Assess the morphology of the red blood cells.
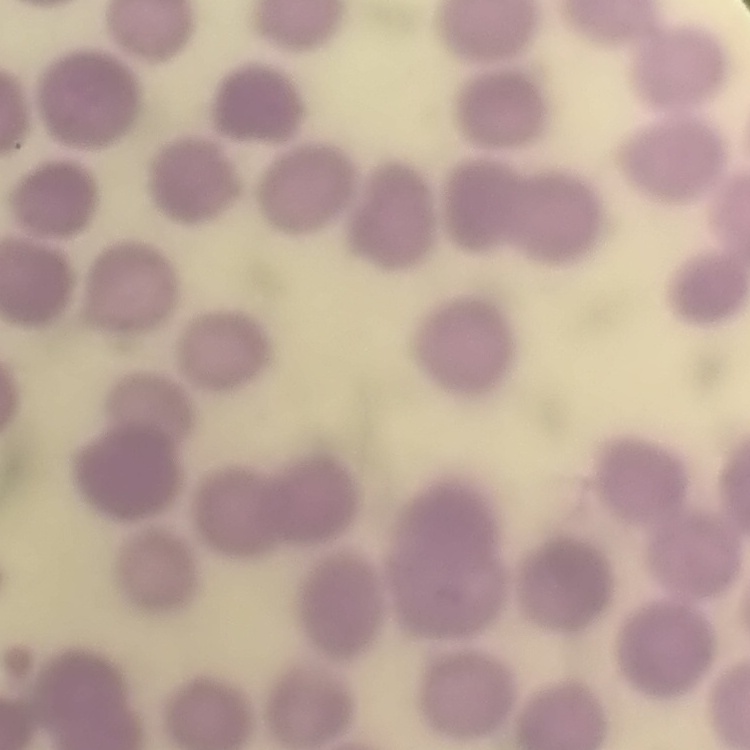

They show no rouleaux formation.

Thin blood film. One tile cut from a larger photomicrograph. Stained with either Field's or Giemsa.